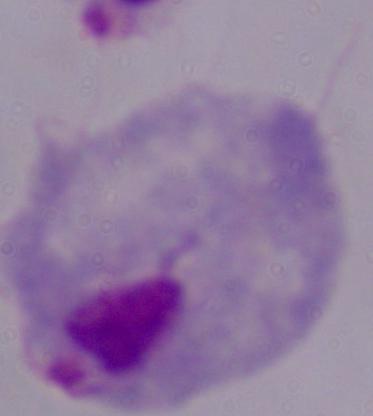

identification: trichomonad
magnification: 1000x
modality: micrograph